Name the parasite shown.
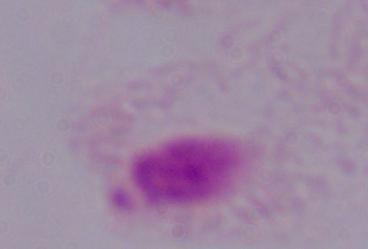

A trichomonad.

Summary:
  - Modality: micrograph
  - Magnification: 1000x